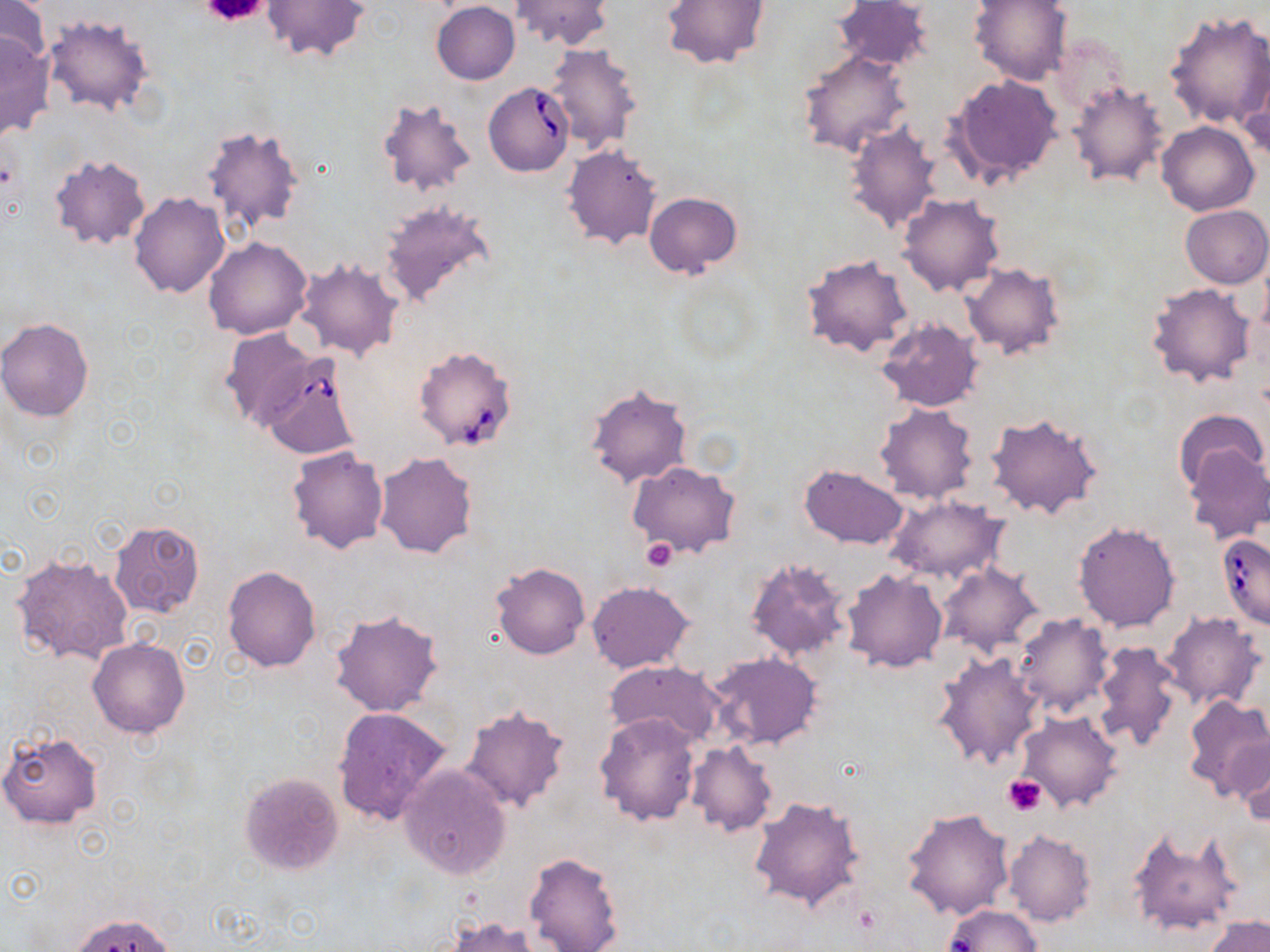
slide-level diagnosis = Babesia divergens
modality = light microscopy
stain = May-Grünwald-Giemsa
field of view = one of a larger specimen
Babesia divergens-infected red blood cell locations = approximate bounding boxes as (x1,y1)-(x2,y2) corner pairs in pixels: (482,82)-(574,176), (413,345)-(519,452), (257,356)-(364,458), (1217,533)-(1270,629)
magnification = 1000x
image size = 1270×952 pixels
uninfected red blood cell locations = approximate bounding boxes as (x1,y1)-(x2,y2) corner pairs in pixels: (0,0)-(53,71), (260,0)-(373,63), (511,0)-(612,50), (662,0)-(771,68), (833,0)-(933,72), (969,0)-(1073,86), (431,2)-(520,84), (1164,11)-(1270,131), (43,15)-(157,118), (0,32)-(54,140), (545,43)-(644,154), (797,50)-(910,159), (1238,68)-(1270,163), (947,74)-(1063,187), (1068,79)-(1170,189), (376,96)-(477,198), (1157,121)-(1260,216), (843,122)-(943,233), (201,123)-(304,234), (561,143)-(664,251), (48,153)-(151,251), (129,191)-(229,297), (644,192)-(741,277), (898,194)-(1005,298), (379,201)-(497,310), (1180,205)-(1270,289), (202,237)-(313,340), (802,255)-(913,359), (295,259)-(403,362), (963,264)-(1063,360), (1147,282)-(1256,389), (0,318)-(96,421), (876,320)-(983,412), (219,327)-(323,431), (585,384)-(693,489), (874,403)-(980,505), (1175,407)-(1266,493), (985,412)-(1103,520), (1182,444)-(1270,543), (286,445)-(390,553), (374,453)-(477,558), (627,460)-(741,559), (799,463)-(910,549), (883,495)-(1008,583), (109,520)-(205,618), (1072,520)-(1182,633), (11,553)-(134,668), (745,556)-(855,664), (491,562)-(589,660), (936,562)-(1044,657), (221,565)-(321,674), (842,570)-(946,673), (587,580)-(695,673), (329,606)-(444,717), (1160,611)-(1267,712), (1013,613)-(1114,719), (89,638)-(189,738), (1093,640)-(1183,753), (932,649)-(1044,771), (706,651)-(824,751), (604,660)-(726,750), (1182,694)-(1270,800), (460,704)-(572,812), (332,706)-(451,826), (1014,710)-(1124,813), (594,711)-(700,825), (0,730)-(104,832), (1231,736)-(1270,827), (686,742)-(778,837), (398,764)-(512,878), (240,772)-(345,875), (748,796)-(865,912), (902,807)-(1015,922), (1127,824)-(1241,936), (1005,829)-(1097,927), (524,851)-(624,952), (942,905)-(1044,951), (70,912)-(177,952), (1206,916)-(1270,952), (446,917)-(540,952)
preparation = thin blood smear
platelet locations = approximate bounding boxes as (x1,y1)-(x2,y2) corner pairs in pixels: (203,0)-(270,24), (643,537)-(678,570), (1003,775)-(1046,814)